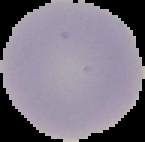
From a thin blood smear. Cell region segmented out of the field of view; the surrounding area is masked to black. Result: negative for Plasmodium parasites. Image is 145×142 pixels.